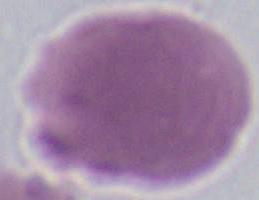
Summary:
  - Magnification: 1000x
  - Modality: micrograph
  - Identification: erythrocyte